Outline each blood parasite and name the species.
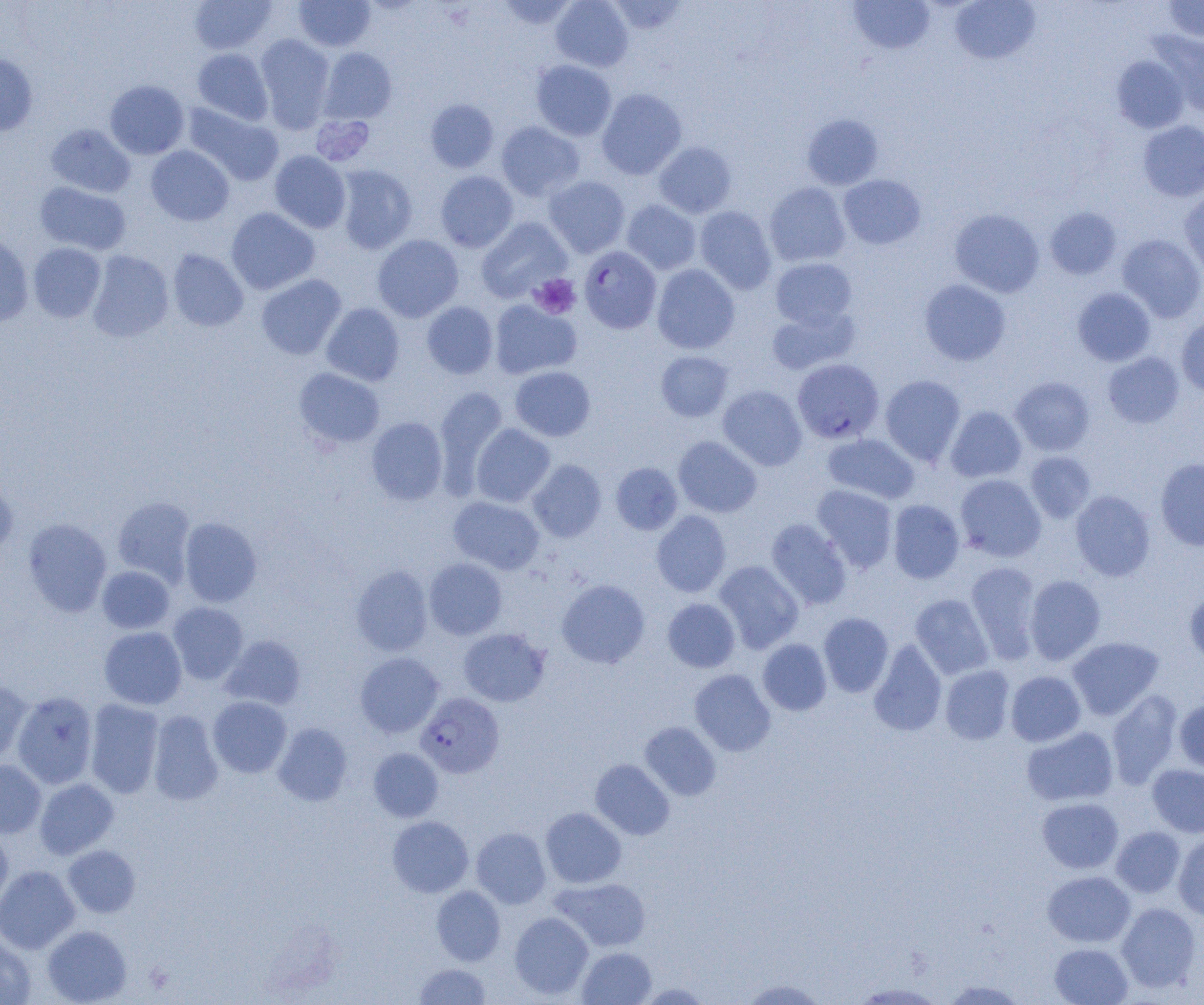
Approximate bounding boxes as (x1, y1, x2, y2) in pixels.
Plasmodium falciparum-infected red blood cells: (579, 246, 661, 334), (792, 358, 884, 443), (416, 693, 504, 777).
No Plasmodium ovale, Plasmodium malariae, Plasmodium vivax, Babesia divergens, or Trypanosoma brucei observed.

Summary:
  - Uninfected red blood cell locations: (189, 0, 277, 54), (294, 0, 375, 52), (496, 0, 578, 31), (550, 0, 633, 71), (607, 0, 688, 35), (849, 0, 935, 55), (1162, 0, 1204, 42), (950, 1, 1040, 64), (1154, 31, 1203, 117), (255, 34, 335, 131), (319, 47, 397, 123), (192, 48, 273, 125), (0, 53, 38, 136), (1112, 55, 1189, 133), (530, 59, 617, 141), (105, 80, 189, 159), (596, 88, 687, 179), (424, 98, 499, 173), (183, 103, 282, 186), (802, 114, 884, 190), (1138, 120, 1204, 202), (496, 121, 585, 201), (46, 124, 135, 198), (654, 141, 737, 218), (145, 145, 234, 226), (269, 150, 351, 233), (335, 165, 417, 254), (435, 171, 518, 253), (838, 174, 926, 249), (544, 176, 630, 258), (34, 181, 131, 255), (764, 182, 851, 267), (1179, 192, 1204, 279), (621, 200, 701, 275), (694, 206, 776, 294), (226, 207, 320, 295), (1044, 207, 1122, 280), (949, 209, 1044, 298), (476, 217, 572, 302), (0, 233, 34, 327), (1117, 234, 1204, 322), (372, 235, 463, 322), (28, 243, 106, 323), (167, 249, 248, 332), (87, 250, 174, 342), (770, 257, 857, 329), (652, 264, 740, 354), (256, 274, 346, 360), (919, 279, 1011, 366), (1072, 287, 1156, 366), (489, 299, 581, 380), (422, 302, 498, 379), (321, 303, 405, 387), (767, 306, 860, 374), (1176, 315, 1204, 397), (656, 351, 733, 422), (1102, 352, 1184, 428), (510, 366, 596, 441), (294, 367, 384, 448), (880, 375, 966, 466), (1010, 377, 1095, 456), (717, 385, 807, 470), (433, 386, 508, 492), (945, 406, 1027, 482), (366, 417, 448, 505), (471, 423, 555, 507), (822, 433, 920, 504), (673, 436, 762, 517), (1025, 451, 1097, 523), (1155, 458, 1204, 550), (528, 460, 607, 542), (611, 462, 683, 535), (955, 474, 1046, 562), (0, 478, 18, 559), (812, 484, 898, 573), (1070, 490, 1155, 581), (112, 496, 196, 586), (448, 496, 545, 574), (888, 499, 964, 583), (651, 510, 731, 597), (179, 517, 263, 607), (23, 518, 112, 616), (766, 518, 851, 609), (424, 558, 507, 640), (714, 560, 804, 653), (966, 561, 1041, 662), (351, 565, 433, 656), (97, 566, 175, 634), (1024, 574, 1106, 665), (556, 579, 650, 668), (1184, 588, 1204, 666), (910, 594, 993, 679), (662, 598, 740, 672), (168, 602, 248, 684), (818, 612, 893, 697), (99, 626, 187, 710), (458, 628, 550, 706), (221, 635, 306, 710), (1066, 636, 1164, 720), (757, 639, 832, 716), (868, 640, 947, 736), (355, 652, 444, 737), (940, 665, 1015, 745), (689, 669, 776, 756), (1006, 670, 1086, 746), (0, 679, 33, 764), (1106, 690, 1182, 789), (11, 692, 98, 789), (207, 696, 292, 778), (1174, 698, 1204, 773), (84, 699, 164, 798), (148, 710, 224, 806), (639, 722, 721, 801), (273, 723, 352, 806), (1021, 726, 1118, 806), (368, 748, 444, 822), (590, 759, 674, 840), (0, 760, 46, 838), (1147, 764, 1204, 837), (35, 778, 118, 859), (1037, 798, 1123, 873), (540, 807, 626, 888), (387, 816, 473, 897), (1111, 826, 1185, 897), (471, 827, 551, 909), (0, 828, 13, 909), (1173, 832, 1204, 920), (63, 845, 140, 918), (0, 865, 80, 954), (1042, 871, 1135, 947), (551, 877, 651, 952), (431, 886, 505, 966), (1116, 903, 1201, 992), (509, 912, 593, 999), (42, 925, 131, 1005), (0, 934, 36, 1005), (1049, 943, 1133, 1005), (577, 947, 656, 1004), (413, 963, 492, 1004), (737, 978, 829, 1004), (941, 979, 1028, 1004), (634, 982, 712, 1004), (848, 982, 948, 1004)
  - Platelet locations: (311, 114, 375, 167), (529, 274, 581, 319)
  - Slide-level diagnosis: Plasmodium falciparum
  - Field of view: one of a larger specimen
  - Magnification: 1000x
  - Preparation: thin blood smear
  - Modality: optical microscopy
  - Image size: 1204×1005 pixels